Report the malaria status of this cell.
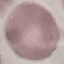

Uninfected.

Acquired by smartphone through the microscope eyepiece. Thin blood film. Cell patch, automatically extracted from a larger field of view and resized to 64 × 64 pixels. Giemsa stain.